Give the extent of all Plasmodium vivax-infected red blood cells.
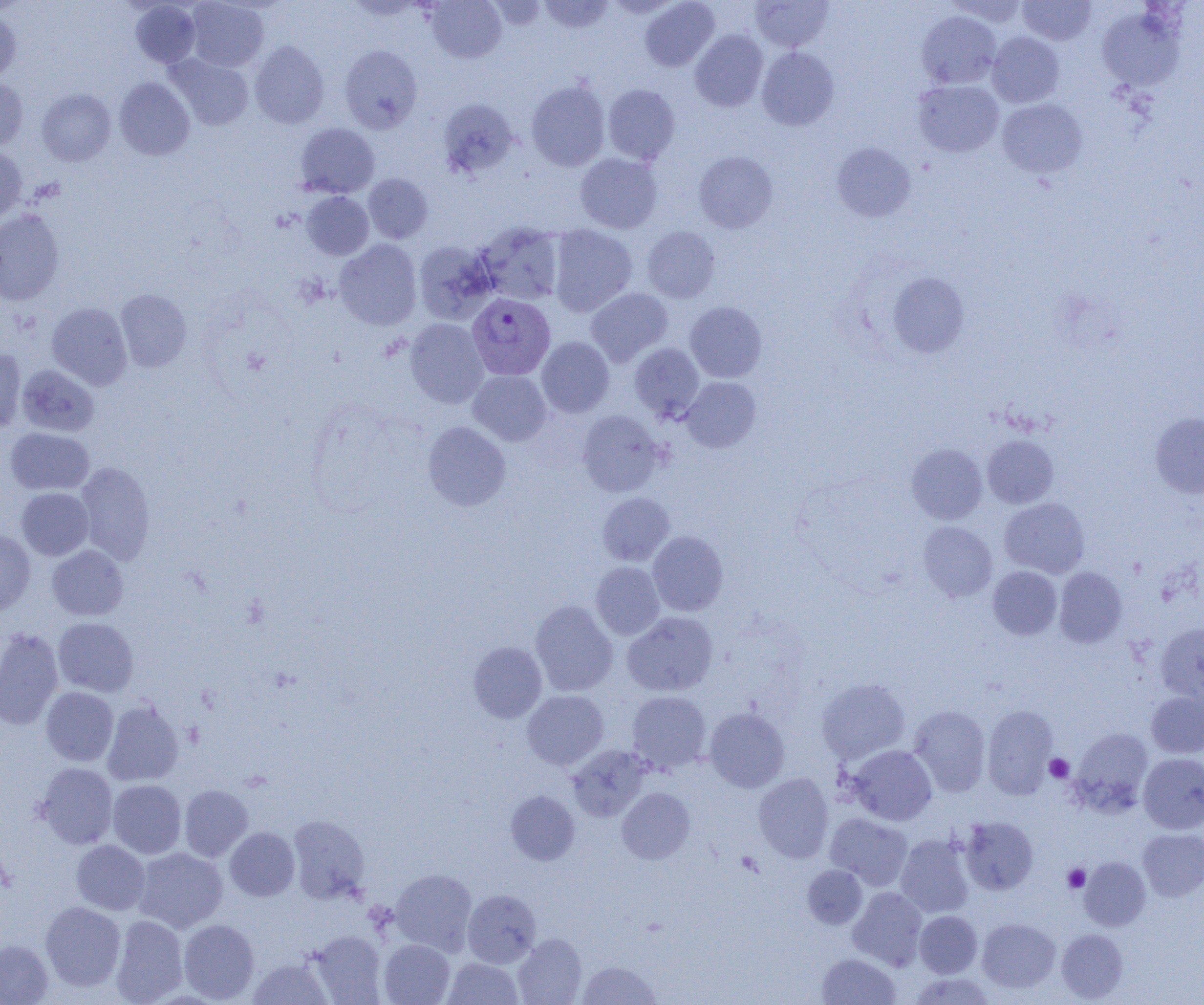
Approximate bounding boxes as [x1, y1, x2, y2] in pixels.
Plasmodium vivax-infected red blood cells: [467, 293, 555, 380].

Platelet locations: [1045, 754, 1074, 782], [1063, 864, 1090, 892]. Uninfected red blood cell locations: [425, 0, 506, 63], [538, 0, 614, 34], [640, 0, 719, 71], [945, 0, 1028, 26], [186, 1, 268, 71], [487, 1, 547, 31], [751, 1, 834, 51], [1018, 1, 1096, 46], [130, 2, 201, 68], [1096, 6, 1184, 91], [0, 8, 21, 81], [916, 11, 1001, 89], [690, 29, 768, 112], [987, 32, 1064, 108], [249, 41, 329, 129], [339, 45, 423, 133], [756, 47, 839, 131], [167, 54, 254, 131], [0, 76, 28, 152], [114, 77, 195, 160], [526, 79, 610, 171], [913, 80, 1004, 157], [603, 84, 680, 164], [37, 89, 115, 166], [913, 91, 1088, 163], [438, 98, 519, 179], [997, 98, 1087, 178], [295, 123, 379, 198], [831, 142, 916, 222], [0, 146, 26, 223], [694, 151, 778, 233], [575, 153, 663, 234], [363, 174, 433, 243], [302, 192, 374, 260], [0, 209, 64, 305], [475, 221, 564, 305], [548, 225, 637, 317], [641, 225, 720, 302], [334, 239, 422, 330], [413, 240, 498, 325], [887, 271, 970, 359], [586, 288, 673, 366], [115, 289, 192, 372], [685, 301, 767, 382], [47, 302, 132, 390], [405, 318, 489, 408], [536, 337, 614, 418], [629, 343, 704, 421], [0, 348, 27, 433], [17, 364, 99, 436], [468, 370, 552, 445], [681, 377, 761, 453], [577, 410, 664, 496], [1150, 412, 1204, 499], [422, 421, 511, 511], [4, 428, 94, 495], [982, 435, 1058, 508], [907, 443, 987, 524], [75, 461, 155, 565], [17, 487, 93, 560], [597, 492, 674, 566], [999, 498, 1089, 578], [918, 521, 997, 602], [0, 530, 35, 616], [648, 531, 728, 616], [47, 545, 128, 620], [591, 562, 664, 639], [988, 566, 1062, 640], [1054, 567, 1127, 647], [530, 600, 618, 696], [622, 611, 718, 696], [53, 617, 138, 697], [1156, 622, 1204, 703], [0, 628, 64, 730], [468, 641, 547, 723], [817, 677, 910, 764], [41, 687, 118, 766], [522, 690, 608, 770], [626, 690, 712, 773], [1146, 691, 1204, 758], [102, 699, 184, 786], [983, 704, 1058, 799], [705, 706, 789, 792], [908, 706, 991, 796], [1071, 727, 1153, 812], [566, 744, 651, 821], [847, 745, 936, 825], [1138, 753, 1204, 834], [36, 763, 118, 848], [753, 772, 833, 863], [107, 779, 186, 858], [179, 784, 252, 862], [617, 787, 695, 864], [506, 790, 579, 865], [825, 813, 913, 889], [288, 815, 369, 903], [959, 816, 1038, 895], [225, 827, 299, 901], [1138, 829, 1204, 901], [895, 834, 974, 918], [71, 840, 150, 914], [133, 847, 228, 933], [1079, 857, 1151, 931], [802, 865, 867, 929], [390, 869, 476, 956], [848, 887, 927, 970], [463, 889, 541, 967], [40, 901, 125, 990], [914, 910, 982, 977], [110, 915, 187, 1004], [977, 918, 1060, 993], [178, 919, 259, 1003], [1056, 929, 1128, 1002], [309, 931, 387, 1003], [513, 934, 586, 1005], [0, 939, 53, 1005], [379, 939, 454, 1005], [816, 952, 901, 1004], [443, 957, 523, 1004], [247, 958, 332, 1005], [577, 961, 661, 1004], [908, 972, 996, 1004]. Slide-level diagnosis: Plasmodium vivax. Single field of view. Captured at 1000x magnification. Thin blood film. Optical microscopy. Image is 1204×1005 pixels.